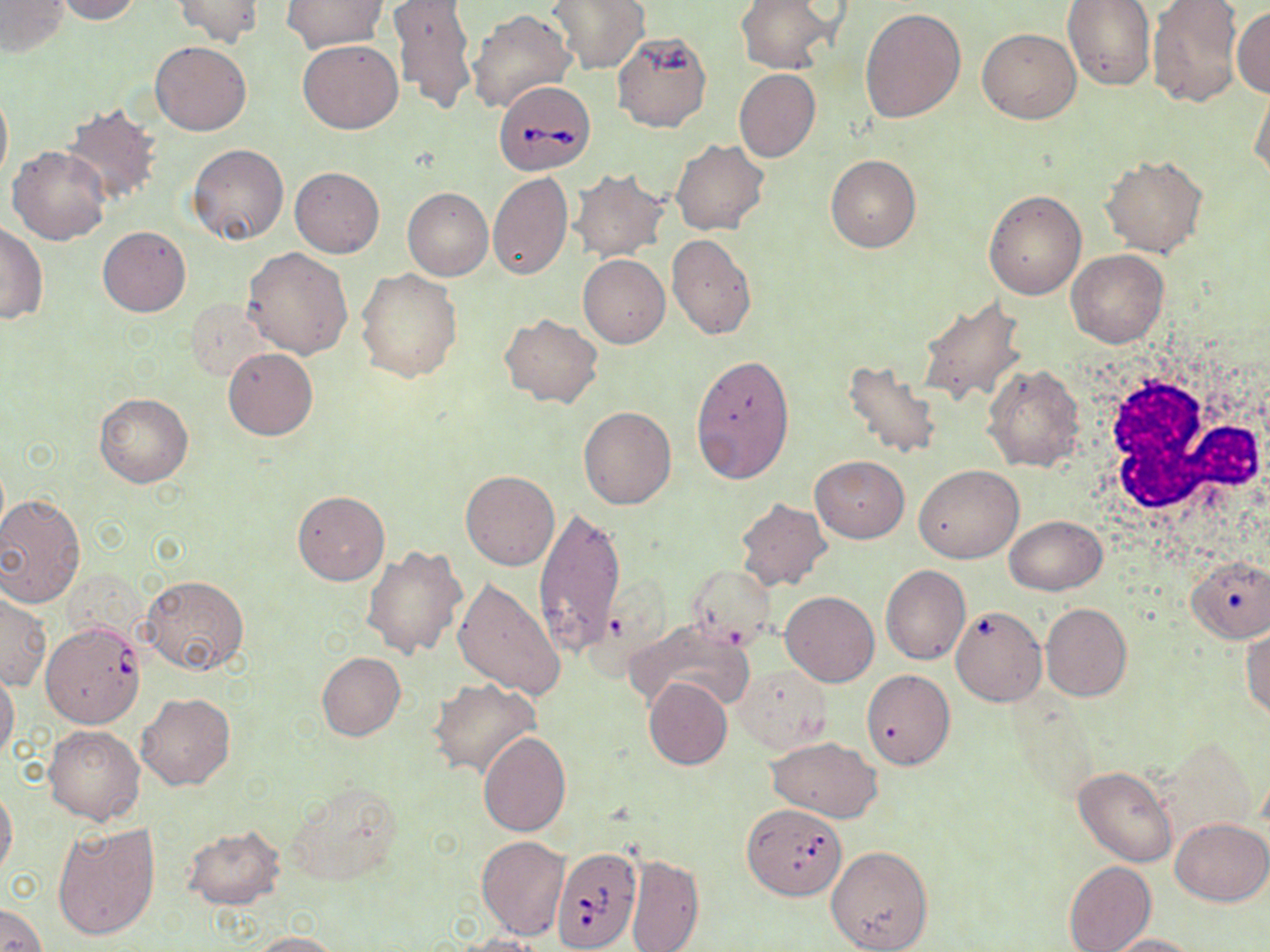

Summary:
  - Coordinate format: approximate bounding boxes as (x1, y1, x2, y2) in pixels
  - Babesia divergens-infected red blood cell locations: (496, 85, 596, 175), (42, 621, 143, 728), (744, 808, 846, 904), (551, 846, 641, 951)
  - White blood cell locations: (1087, 357, 1267, 531)
  - Uninfected red blood cell locations: (1, 0, 69, 57), (54, 0, 142, 24), (171, 0, 264, 47), (735, 0, 837, 74), (1063, 0, 1154, 89), (1145, 0, 1244, 107), (281, 1, 388, 53), (388, 1, 477, 115), (547, 1, 649, 74), (1232, 6, 1270, 97), (467, 8, 577, 115), (861, 8, 966, 124), (976, 27, 1081, 124), (612, 31, 712, 133), (151, 40, 250, 135), (297, 40, 404, 134), (734, 68, 822, 162), (1248, 81, 1270, 184), (0, 83, 12, 189), (61, 103, 164, 208), (671, 140, 769, 236), (187, 144, 289, 246), (7, 146, 110, 245), (1100, 152, 1208, 257), (826, 154, 921, 252), (290, 165, 384, 257), (569, 169, 668, 260), (487, 173, 573, 281), (403, 187, 493, 280), (984, 188, 1087, 299), (0, 222, 48, 324), (98, 226, 190, 316), (667, 233, 756, 338), (243, 247, 353, 360), (1066, 248, 1168, 347), (578, 253, 670, 347), (355, 268, 461, 382), (916, 297, 1026, 405), (188, 300, 276, 381), (499, 313, 602, 407), (223, 347, 318, 440), (690, 353, 796, 483), (843, 358, 944, 461), (982, 362, 1087, 473), (94, 393, 194, 487), (579, 405, 677, 509), (810, 456, 909, 542), (914, 464, 1025, 563), (461, 470, 559, 570), (292, 490, 389, 586), (0, 495, 84, 607), (734, 498, 831, 591), (534, 503, 626, 658), (1003, 516, 1107, 595), (360, 545, 467, 660), (1188, 554, 1269, 642), (686, 565, 776, 645), (881, 565, 971, 664), (142, 574, 249, 675), (452, 577, 567, 700), (781, 590, 879, 687), (1, 593, 51, 690), (1040, 603, 1131, 702), (951, 605, 1047, 705), (625, 620, 757, 715), (1241, 627, 1270, 721), (317, 653, 405, 740), (734, 665, 831, 753), (862, 669, 955, 769), (0, 670, 20, 761), (428, 677, 540, 778), (643, 677, 732, 769), (136, 692, 235, 791), (443, 697, 565, 817), (43, 724, 145, 824), (478, 731, 572, 836), (765, 737, 882, 822), (1074, 766, 1175, 866), (281, 782, 403, 887), (0, 786, 18, 881), (1170, 817, 1268, 905), (51, 821, 159, 941), (181, 826, 285, 909), (477, 836, 569, 939), (826, 845, 935, 952), (627, 852, 704, 952), (1063, 861, 1156, 952), (0, 904, 46, 952), (247, 931, 340, 951), (453, 934, 544, 952), (1102, 934, 1201, 952)
  - Slide-level diagnosis: Babesia divergens
  - Image size: 1270×952 pixels
  - Preparation: thin blood film
  - Magnification: 1000x
  - Field of view: one of a larger specimen
  - Modality: light microscopy
  - Stain: May-Grünwald-Giemsa